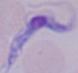
identification = trypanosome
magnification = 1000x
modality = photomicrograph